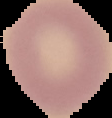

Summary:
  - Image size: 112×118 pixels
  - Preparation: thin blood smear
  - Malaria status: uninfected
  - Image type: segmented cell region on a black background